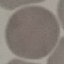
Summary:
  - Malaria status: uninfected
  - Image type: cell patch, automatically extracted from a larger field of view and resized to 64 × 64 pixels
  - Stain: Giemsa
  - Capture: smartphone camera at the microscope eyepiece
  - Preparation: thin blood film